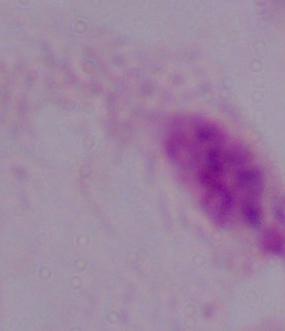
modality = photomicrograph
identification = trichomonad
magnification = 1000x